Give the extent of all Plasmodium malariae-infected red blood cells.
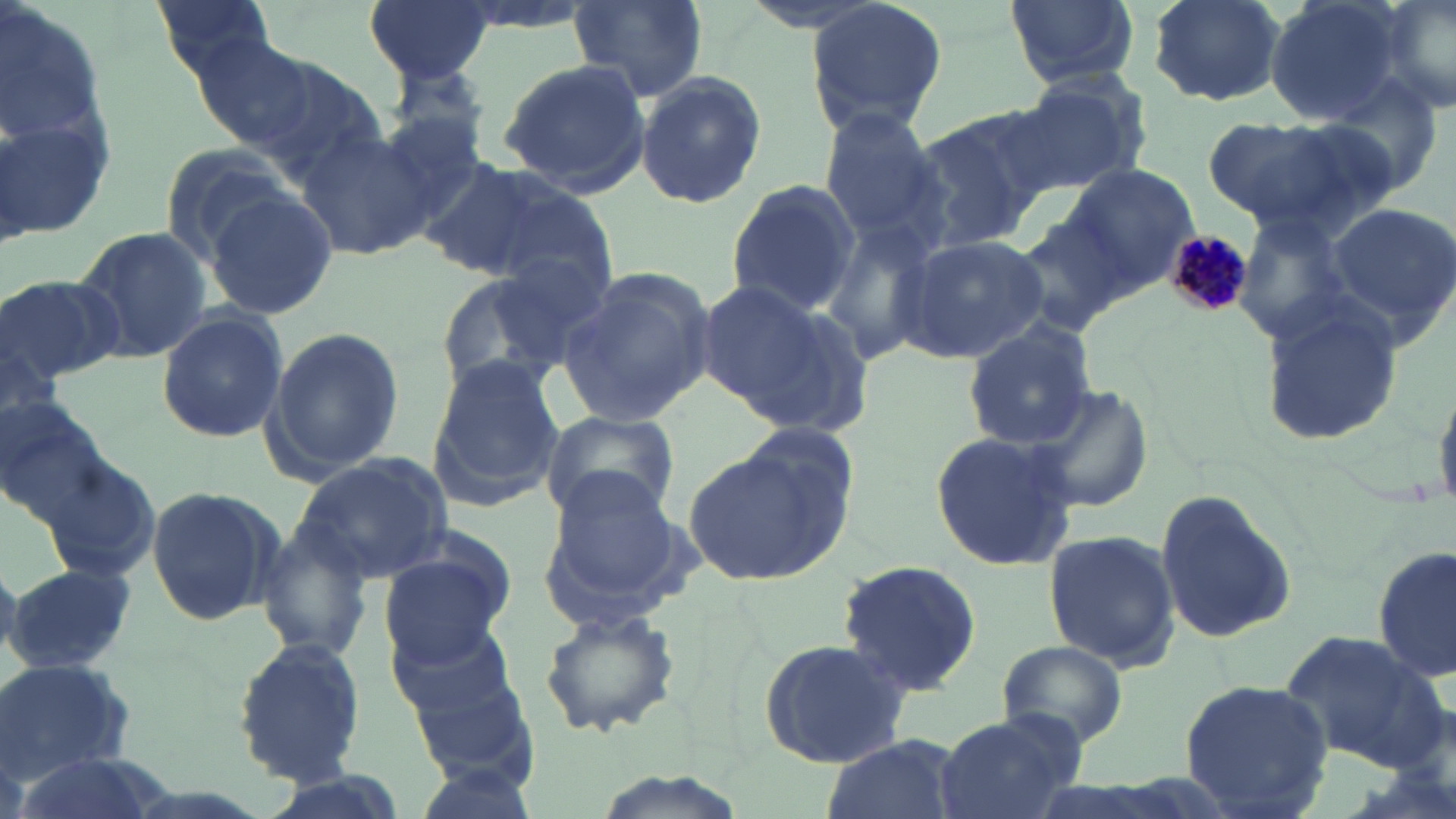
Approximate bounding boxes as named x1/y1/x2/y2 corners in pixels.
Plasmodium malariae-infected red blood cells: (x1=1164, y1=227, x2=1253, y2=320).

slide_level_diagnosis: Plasmodium malariae
stain: May-Grünwald-Giemsa
modality: light microscopy
image_size: 1456×819 pixels
preparation: thin blood film
uninfected_red_blood_cell_locations: 'approximate bounding boxes as named x1/y1/x2/y2 corners in pixels: (x1=150, y1=0, x2=278, y2=74), (x1=366, y1=0, x2=491, y2=82), (x1=444, y1=0, x2=597, y2=34), (x1=803, y1=0, x2=949, y2=138), (x1=1001, y1=0, x2=1141, y2=90), (x1=1142, y1=0, x2=1290, y2=106), (x1=1263, y1=0, x2=1407, y2=125), (x1=1374, y1=0, x2=1455, y2=120), (x1=1, y1=1, x2=119, y2=242), (x1=570, y1=1, x2=705, y2=102), (x1=192, y1=35, x2=323, y2=156), (x1=498, y1=57, x2=649, y2=195), (x1=248, y1=60, x2=388, y2=186), (x1=391, y1=60, x2=495, y2=149), (x1=633, y1=72, x2=766, y2=211), (x1=1005, y1=75, x2=1147, y2=197), (x1=366, y1=109, x2=490, y2=228), (x1=816, y1=109, x2=948, y2=247), (x1=904, y1=114, x2=1043, y2=252), (x1=1210, y1=114, x2=1392, y2=239), (x1=297, y1=126, x2=438, y2=262), (x1=157, y1=144, x2=297, y2=263), (x1=416, y1=157, x2=567, y2=280), (x1=1057, y1=158, x2=1200, y2=292), (x1=723, y1=179, x2=862, y2=318), (x1=482, y1=181, x2=620, y2=306), (x1=201, y1=190, x2=338, y2=320), (x1=1320, y1=199, x2=1456, y2=341), (x1=1014, y1=205, x2=1141, y2=335), (x1=1230, y1=214, x2=1358, y2=345), (x1=817, y1=220, x2=942, y2=368), (x1=71, y1=228, x2=211, y2=362), (x1=897, y1=234, x2=1048, y2=361), (x1=554, y1=268, x2=715, y2=427), (x1=435, y1=270, x2=581, y2=400), (x1=1, y1=274, x2=124, y2=387), (x1=699, y1=279, x2=871, y2=437), (x1=1257, y1=295, x2=1403, y2=446), (x1=155, y1=306, x2=289, y2=444), (x1=962, y1=322, x2=1098, y2=451), (x1=265, y1=327, x2=404, y2=479), (x1=2, y1=334, x2=64, y2=445), (x1=428, y1=357, x2=562, y2=508), (x1=1019, y1=384, x2=1153, y2=513), (x1=0, y1=387, x2=112, y2=521), (x1=540, y1=407, x2=681, y2=524), (x1=929, y1=430, x2=1083, y2=573), (x1=682, y1=435, x2=854, y2=586), (x1=294, y1=452, x2=452, y2=580), (x1=536, y1=467, x2=697, y2=627), (x1=144, y1=484, x2=282, y2=626), (x1=1153, y1=487, x2=1297, y2=648), (x1=255, y1=524, x2=372, y2=662), (x1=1040, y1=529, x2=1180, y2=671), (x1=376, y1=542, x2=512, y2=668), (x1=1374, y1=544, x2=1454, y2=686), (x1=837, y1=561, x2=983, y2=694), (x1=4, y1=562, x2=138, y2=677), (x1=538, y1=603, x2=683, y2=738), (x1=386, y1=613, x2=527, y2=738), (x1=1279, y1=631, x2=1450, y2=770), (x1=758, y1=636, x2=912, y2=769), (x1=231, y1=638, x2=368, y2=786), (x1=995, y1=639, x2=1128, y2=750), (x1=0, y1=660, x2=136, y2=786), (x1=1177, y1=678, x2=1334, y2=819), (x1=933, y1=713, x2=1080, y2=819), (x1=820, y1=735, x2=964, y2=819), (x1=7, y1=750, x2=161, y2=819), (x1=255, y1=772, x2=404, y2=819)'
field_of_view: single
magnification: 1000x